Assess this cell for malaria.
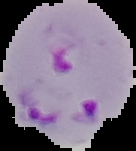
It is parasitized.

Summary:
  - Image size: 136×151 pixels
  - Preparation: thin blood film
  - Image type: segmented cell region on a black background